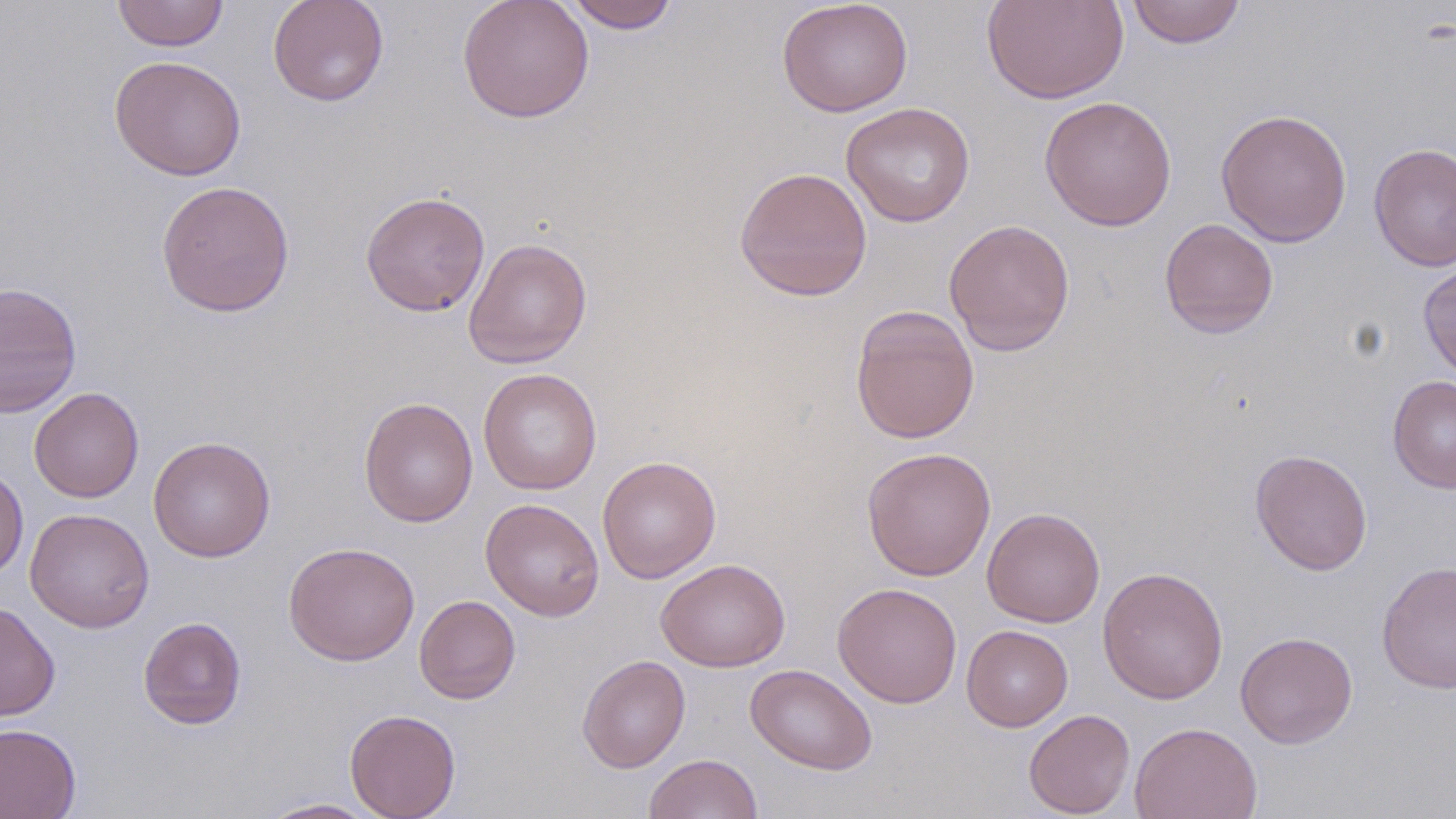

Approximate bounding boxes as (x1,y1)-(x2,y2) corner pairs in pixels. Uninfected red blood cell locations: (111,0)-(230,52), (267,0)-(389,107), (456,0)-(594,124), (563,0)-(680,33), (776,0)-(913,117), (1125,0)-(1247,48), (981,1)-(1129,104), (109,55)-(247,181), (1039,94)-(1177,232), (841,102)-(976,227), (1215,108)-(1352,248), (1368,143)-(1456,272), (734,167)-(873,301), (155,180)-(295,318), (360,190)-(491,317), (943,218)-(1075,356), (1159,218)-(1279,338), (463,238)-(593,368), (1418,259)-(1456,383), (0,281)-(82,418), (850,305)-(980,444), (478,368)-(602,495), (1387,374)-(1456,494), (29,387)-(144,503), (358,397)-(479,527), (148,436)-(276,562), (861,446)-(996,581), (1249,448)-(1373,575), (597,455)-(721,583), (0,464)-(29,580), (480,498)-(604,621), (981,506)-(1105,627), (24,507)-(154,634), (282,541)-(420,666), (655,558)-(791,673), (1377,560)-(1456,694), (1097,565)-(1229,705), (832,582)-(962,709), (414,595)-(521,704), (0,601)-(60,722), (138,616)-(247,730), (961,625)-(1073,731), (1235,631)-(1358,748), (577,654)-(690,773), (745,663)-(878,774), (344,708)-(461,819), (1024,709)-(1135,818), (1130,721)-(1263,819), (0,723)-(81,819), (644,753)-(763,819), (255,798)-(386,818). Slide-level diagnosis: no evidence of blood parasites. Image is 1456×819 pixels. May-Grünwald-Giemsa stain. Light microscopy. Captured at 1000x magnification. Thin blood smear. Single field of view.